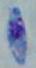
Micrograph. 1000x magnification. Toxoplasma gondii is shown.